Point out every malaria parasite and every leukocyte.
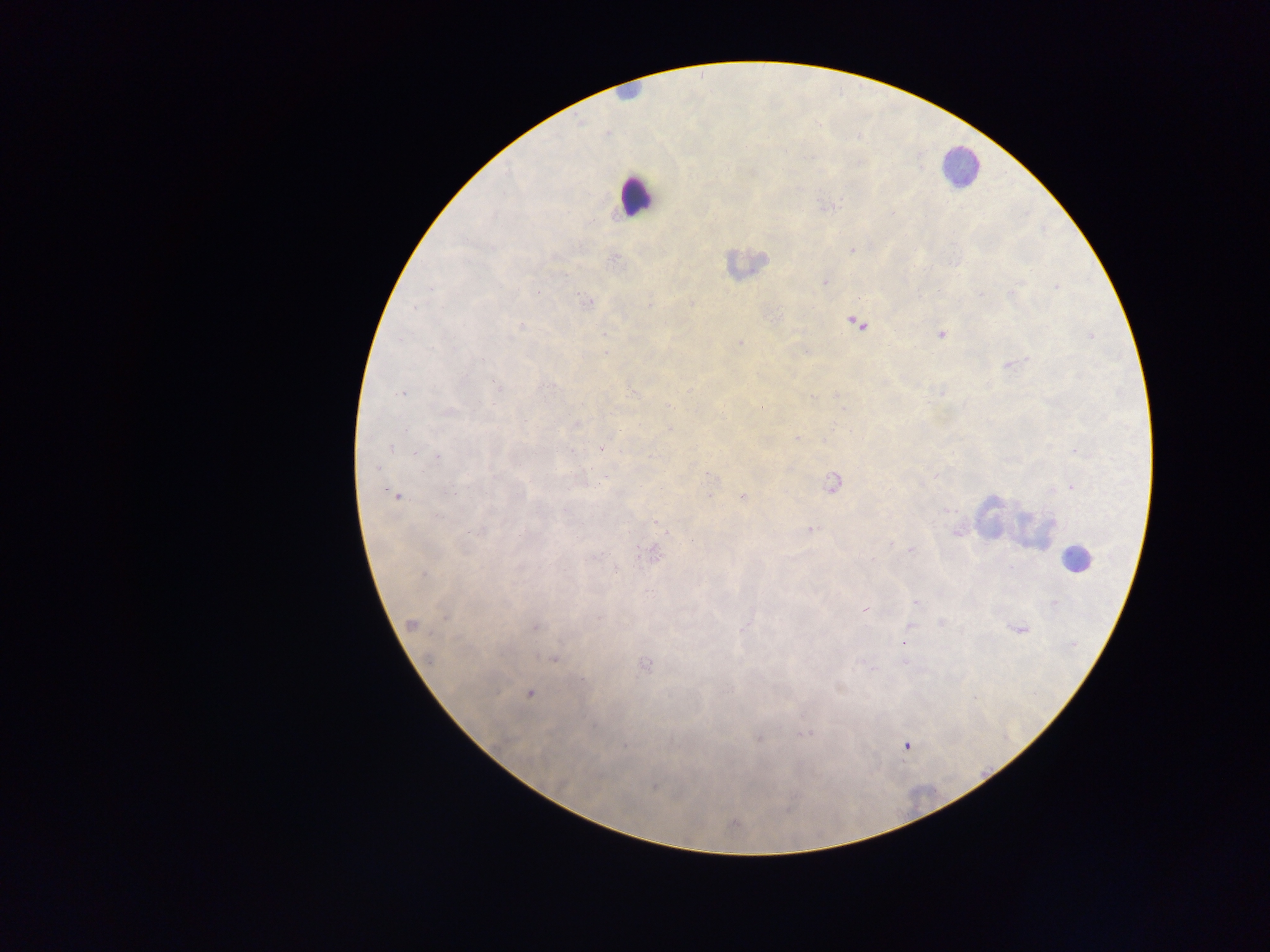
Approximate centers as {x, y} in pixels.
Malaria parasites: {893, 213}, {852, 249}, {614, 260}, {825, 281}, {1012, 294}, {691, 303}, {587, 304}, {856, 323}, {521, 327}, {940, 335}, {739, 343}, {806, 351}, {1010, 364}, {402, 393}, {835, 393}, {446, 410}, {574, 424}, {670, 428}, {797, 439}, {391, 447}, {601, 448}, {711, 475}, {606, 478}, {833, 483}, {396, 495}, {742, 497}, {811, 530}, {910, 549}, {652, 552}, {916, 602}, {1053, 603}, {864, 609}, {940, 622}, {411, 624}, {535, 627}, {1018, 628}, {903, 644}, {552, 657}, {644, 663}, {838, 688}, {529, 693}, {808, 734}, {758, 737}, {906, 746}, {654, 785}, {733, 823}.
Leukocytes: {629, 93}, {960, 166}, {635, 195}, {745, 264}, {1012, 520}, {1074, 558}, {920, 799}.

preparation = thick blood film
image size = 1270×952 pixels
country = Ghana
field of view = single
capture = mobile-phone photograph through a microscope